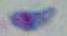
Summary:
  - Magnification: 1000x
  - Identification: Toxoplasma gondii
  - Modality: micrograph